Assess the morphology of the erythrocytes.
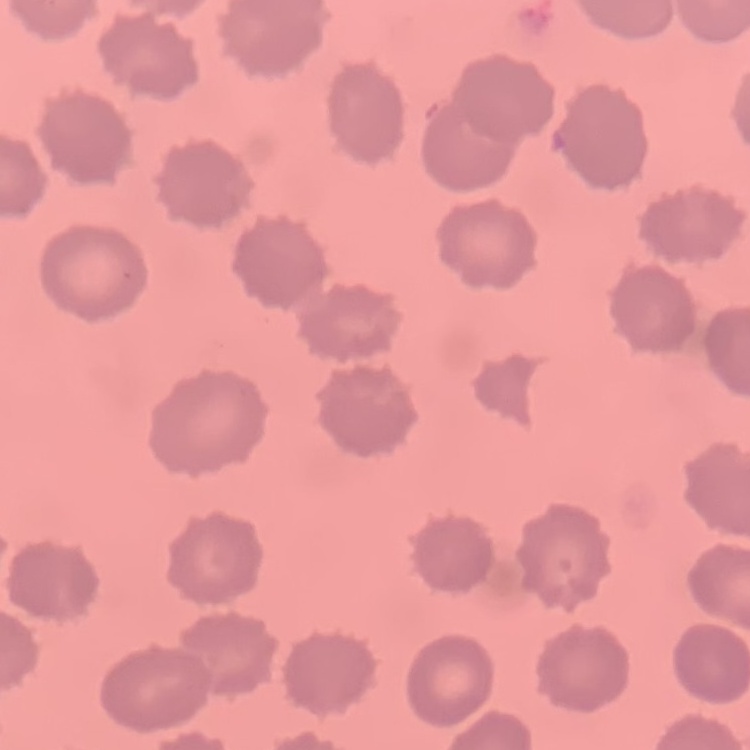

No rouleaux formation.

Thin blood smear. Square crop of a larger photomicrograph. Stained with either Field's or Giemsa.